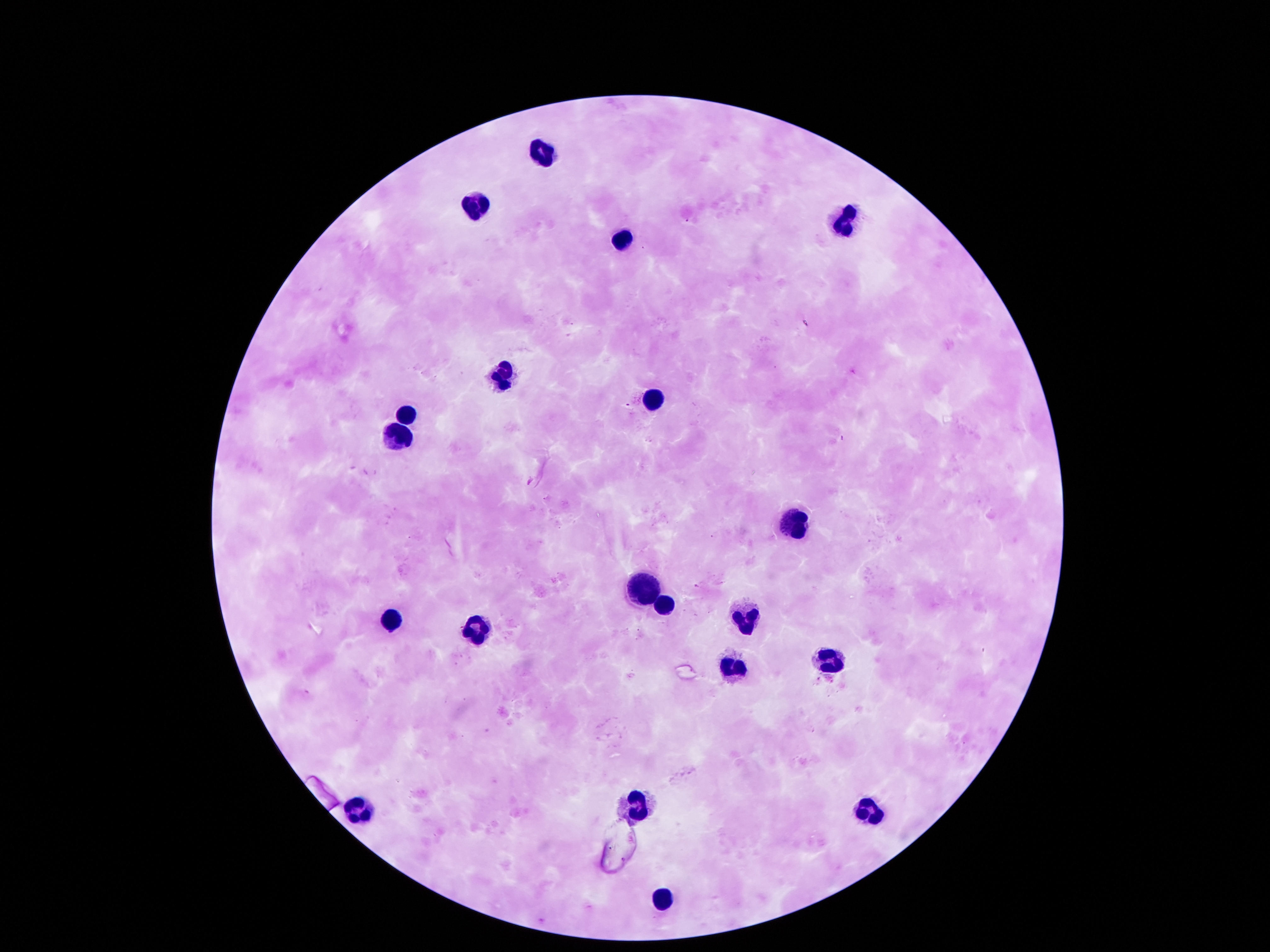

image size = 1270×952 pixels
patient malaria status = uninfected
leukocyte locations = approximate centers as (x, y) in pixels: (538, 156), (474, 200), (844, 216), (625, 236), (504, 375), (652, 395), (407, 412), (393, 439), (790, 520), (645, 590), (662, 606), (390, 617), (746, 619), (471, 629), (827, 654), (733, 667), (639, 805), (864, 805), (356, 807), (659, 899)
preparation = thick peripheral-blood smear
magnification = 100x
field of view = single
capture = smartphone camera through the microscope eyepiece
stain = Giemsa